Report the malaria status.
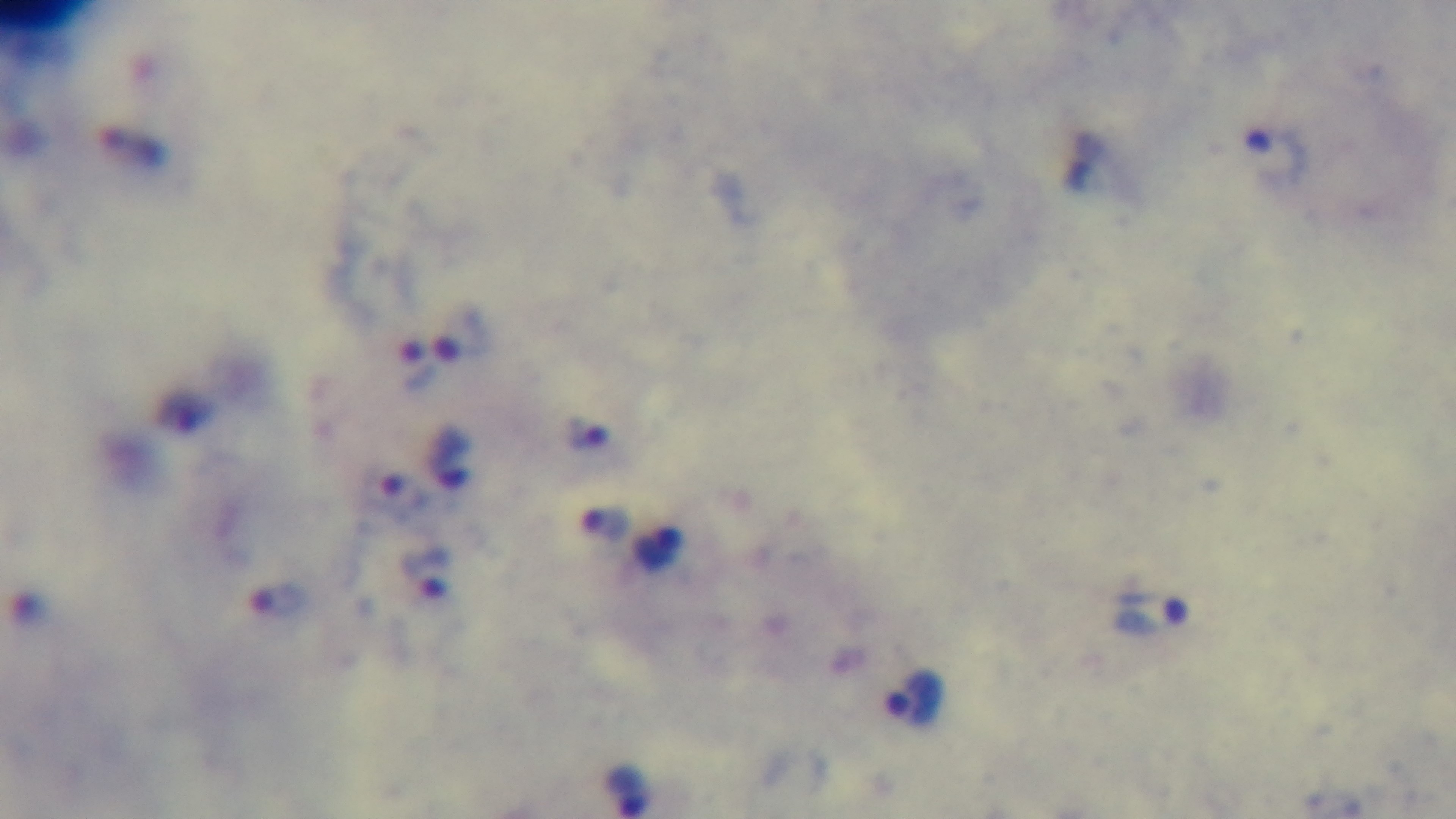

Positive.

field_of_view: single
preparation: thick
capture: mounted 4K digital camera
stain: Giemsa
objective: 100x oil immersion
modality: light microscopy